Locate and identify every blood parasite.
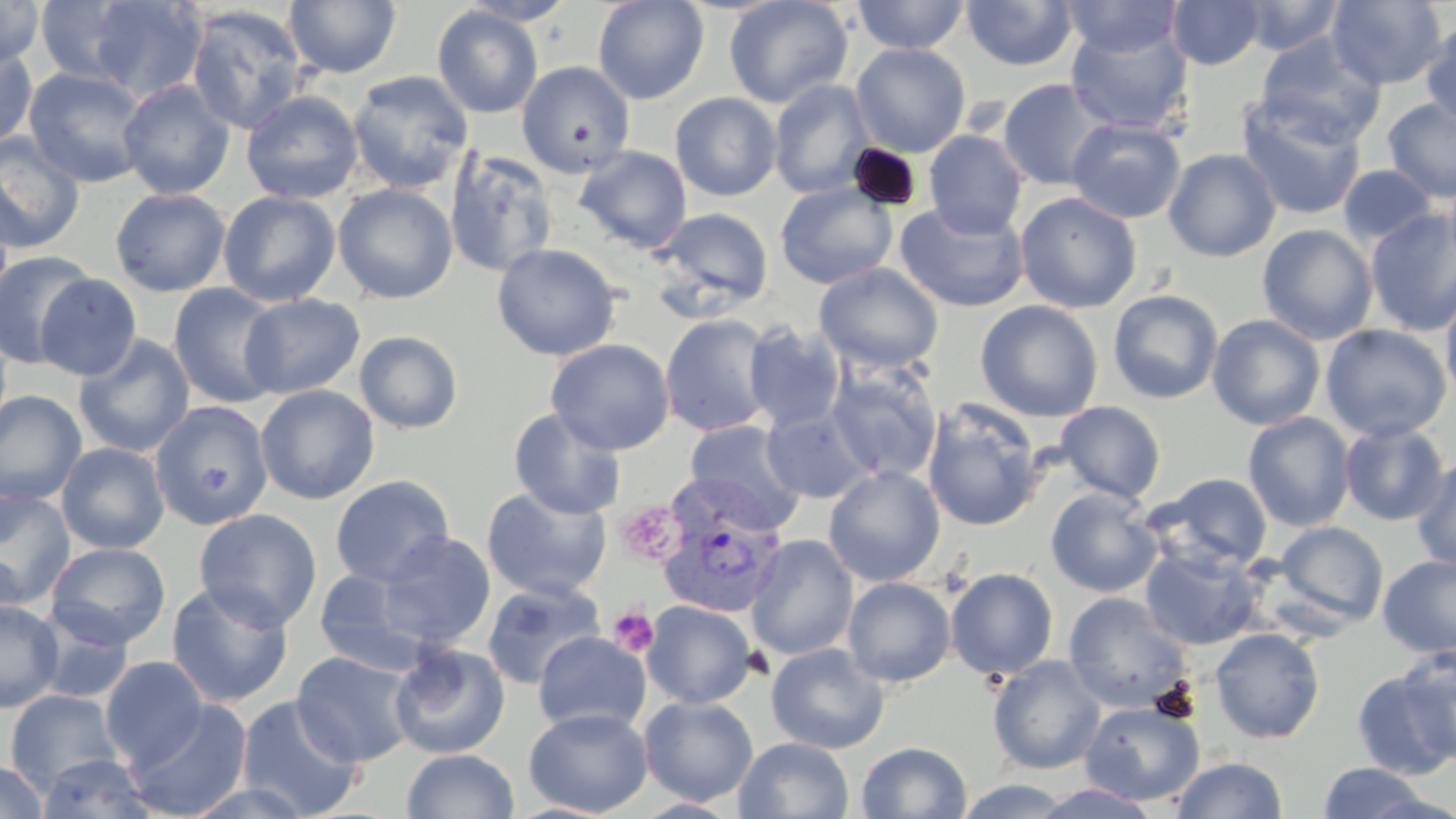

Approximate bounding boxes as (x1, y1, x2, y2) in pixels.
Plasmodium vivax-infected red blood cells: (655, 490, 791, 619).
No Plasmodium falciparum, Plasmodium ovale, Plasmodium malariae, Babesia divergens, or Trypanosoma brucei observed.

Summary:
  - Uninfected red blood cell locations: (34, 0, 146, 87), (284, 0, 402, 78), (458, 0, 578, 26), (593, 0, 709, 104), (723, 0, 853, 109), (851, 0, 971, 54), (1061, 0, 1185, 58), (1167, 0, 1264, 70), (1236, 0, 1346, 56), (1327, 0, 1447, 89), (0, 1, 45, 67), (84, 1, 207, 102), (962, 1, 1079, 71), (185, 5, 309, 135), (433, 5, 543, 119), (1065, 20, 1193, 135), (1421, 21, 1455, 129), (1255, 33, 1386, 148), (850, 43, 970, 156), (0, 44, 39, 152), (516, 60, 636, 178), (23, 67, 153, 189), (347, 70, 474, 194), (997, 78, 1113, 190), (118, 79, 236, 199), (768, 79, 876, 199), (241, 91, 364, 204), (670, 92, 782, 201), (1236, 96, 1366, 221), (1382, 98, 1456, 203), (1066, 117, 1186, 223), (923, 129, 1028, 239), (0, 133, 86, 254), (574, 145, 692, 253), (443, 148, 559, 278), (1163, 148, 1282, 262), (1337, 165, 1438, 247), (775, 181, 897, 290), (332, 183, 458, 304), (110, 187, 231, 296), (218, 190, 341, 306), (1015, 191, 1142, 313), (0, 194, 15, 311), (895, 201, 1030, 313), (653, 207, 773, 312), (1364, 208, 1456, 337), (1257, 224, 1378, 345), (491, 243, 621, 361), (0, 249, 99, 369), (814, 262, 944, 374), (34, 272, 142, 381), (168, 283, 285, 409), (1440, 285, 1456, 408), (1107, 289, 1224, 404), (239, 293, 365, 399), (975, 300, 1103, 422), (660, 313, 776, 437), (1207, 314, 1325, 430), (742, 323, 846, 432), (0, 324, 12, 443), (1320, 324, 1451, 442), (354, 330, 464, 434), (73, 334, 196, 457), (546, 338, 675, 456), (826, 361, 942, 484), (255, 384, 379, 505), (0, 390, 87, 506), (921, 400, 1045, 531), (1055, 400, 1165, 503), (150, 401, 273, 529), (762, 405, 876, 504), (508, 407, 627, 520), (1242, 412, 1355, 531), (683, 421, 806, 532), (1338, 422, 1451, 525), (56, 442, 170, 554), (1411, 456, 1456, 573), (823, 466, 945, 586), (1147, 473, 1274, 571), (330, 475, 455, 587), (481, 486, 612, 601), (1045, 487, 1163, 598), (0, 489, 76, 608), (193, 508, 322, 631), (1273, 521, 1389, 629), (376, 531, 496, 649), (746, 534, 859, 661), (46, 542, 170, 650), (1140, 543, 1265, 651), (0, 550, 24, 631), (1377, 555, 1456, 658), (1375, 556, 1456, 781), (314, 566, 434, 675), (945, 567, 1058, 680), (843, 577, 955, 687), (482, 580, 606, 690), (166, 581, 294, 707), (1062, 591, 1193, 713), (0, 599, 64, 712), (641, 600, 756, 709), (34, 611, 134, 704), (1209, 627, 1325, 743), (533, 632, 651, 735), (389, 642, 510, 759), (766, 642, 890, 753), (1397, 644, 1456, 762), (292, 650, 419, 767), (100, 655, 209, 770), (988, 656, 1106, 775), (1351, 670, 1455, 779), (5, 689, 123, 795), (236, 695, 364, 818), (639, 695, 758, 806), (127, 699, 252, 819), (1079, 700, 1205, 806), (523, 707, 653, 817), (734, 737, 854, 819), (856, 741, 972, 819), (402, 749, 518, 819), (36, 753, 158, 818), (1169, 756, 1288, 818), (0, 759, 49, 819), (1317, 761, 1431, 818), (182, 778, 318, 818), (954, 778, 1075, 818), (1032, 782, 1163, 819)
  - Platelet locations: (615, 501, 684, 566), (608, 604, 659, 657)
  - Slide-level diagnosis: Plasmodium vivax
  - Stain: May-Grünwald-Giemsa
  - Magnification: 1000x
  - Modality: light microscopy
  - Field of view: single
  - Preparation: thin blood smear
  - Image size: 1456×819 pixels